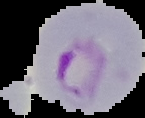

Summary:
  - Preparation: thin blood film
  - Image size: 145×118 pixels
  - Malaria status: parasitized
  - Image type: cell region segmented out of the field of view; surrounding area masked to black